State which parasite is depicted.
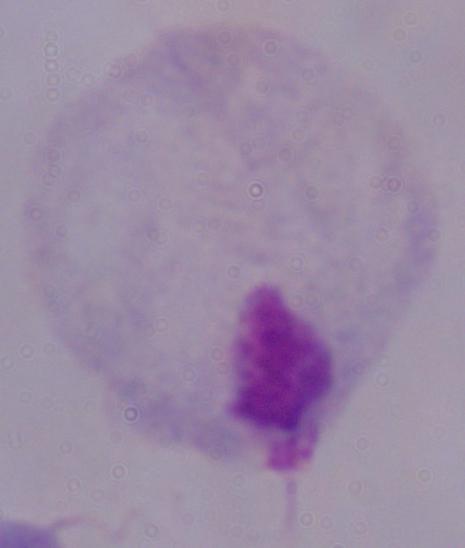

This is a trichomonad.

magnification = 1000x
modality = micrograph